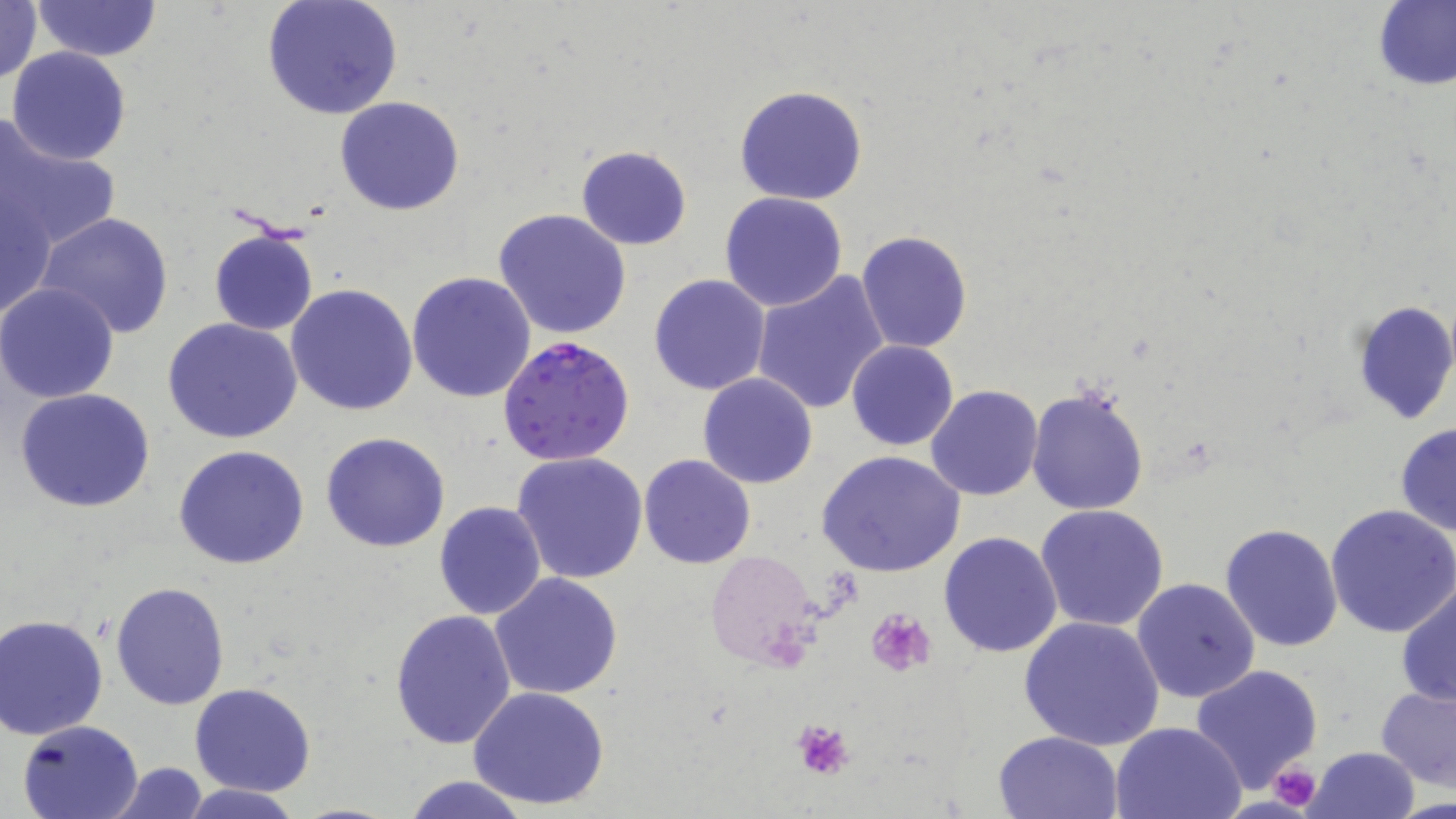 Approximate bounding boxes as (x1, y1, x2, y2) in pixels. Plasmodium falciparum-infected red blood cell locations: (500, 335, 636, 465). Uninfected red blood cell locations: (0, 0, 44, 86), (261, 0, 404, 120), (33, 1, 158, 62), (1375, 1, 1455, 90), (7, 46, 130, 166), (734, 85, 868, 205), (333, 94, 465, 215), (0, 120, 118, 252), (575, 144, 692, 250), (1, 184, 58, 324), (720, 192, 850, 312), (492, 207, 632, 341), (35, 212, 175, 339), (207, 225, 320, 336), (857, 229, 973, 353), (405, 270, 537, 403), (749, 271, 889, 415), (648, 275, 771, 395), (0, 282, 121, 403), (285, 284, 418, 415), (1349, 299, 1456, 426), (161, 317, 303, 444), (847, 340, 960, 452), (697, 373, 819, 489), (925, 384, 1044, 501), (1026, 386, 1150, 516), (14, 388, 157, 514), (669, 410, 805, 551), (1395, 423, 1456, 538), (321, 431, 451, 552), (173, 445, 311, 569), (815, 450, 966, 577), (510, 451, 648, 584), (638, 454, 756, 569), (434, 501, 548, 619), (1036, 504, 1169, 632), (1326, 504, 1456, 637), (1221, 523, 1344, 650), (938, 531, 1065, 658), (704, 549, 823, 671), (490, 572, 624, 701), (1131, 578, 1260, 704), (1395, 578, 1456, 707), (109, 581, 230, 710), (390, 609, 517, 749), (2, 613, 111, 740), (1018, 616, 1164, 750), (1192, 664, 1324, 794), (189, 682, 317, 797), (1376, 685, 1455, 788), (467, 686, 611, 810), (16, 719, 147, 818), (1110, 721, 1246, 818), (993, 728, 1124, 819), (1302, 746, 1421, 819), (107, 762, 209, 818), (399, 775, 536, 819), (178, 783, 304, 819). Platelet locations: (866, 609, 937, 675), (790, 719, 857, 780), (1267, 762, 1323, 809). Slide-level diagnosis: Plasmodium falciparum. Image is 1456×819 pixels. Light microscopy. Captured at 1000x magnification. Thin blood smear. May-Grünwald-Giemsa-stained preparation. Single field of view.